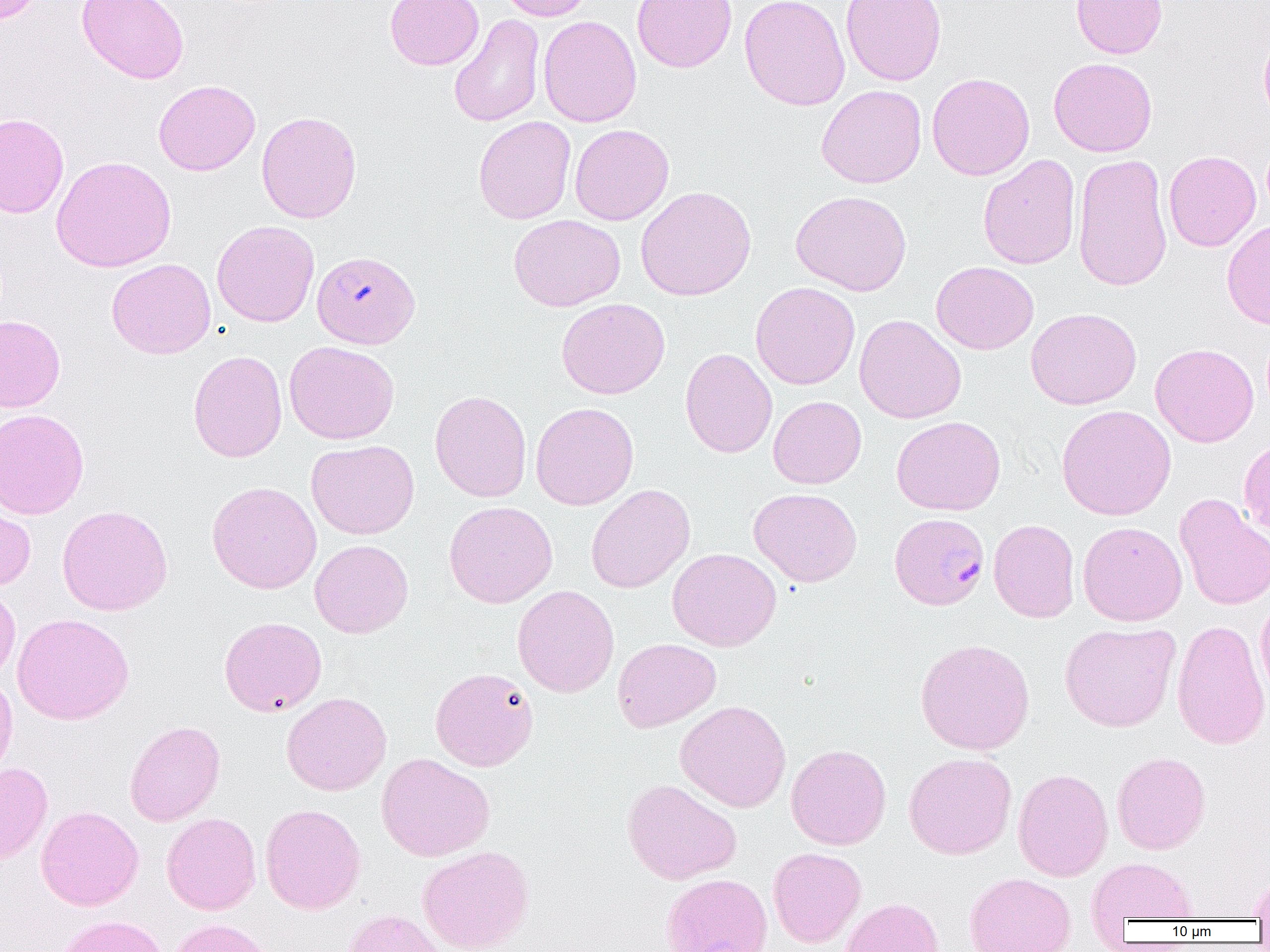

slide_level_diagnosis: Plasmodium falciparum
field_of_view: one of a larger specimen
plasmodium_falciparum_infected_red_blood_cell_locations_subset: 'approximate bounding boxes as [x1, y1, x2, y2] in pixels: [888, 513, 989, 610]'
modality: optical microscopy
preparation: thin blood film
magnification: 1000x
image_size: 1270×952 pixels
uninfected_red_blood_cell_locations_subset: 'approximate bounding boxes as [x1, y1, x2, y2] in pixels: [0, 0, 43, 25], [76, 0, 189, 84], [385, 0, 484, 70], [497, 0, 593, 21], [632, 0, 737, 72], [739, 0, 850, 111], [840, 0, 947, 86], [1071, 0, 1167, 59], [449, 14, 545, 128], [538, 15, 642, 128], [1258, 28, 1270, 127], [1048, 57, 1157, 157], [926, 72, 1035, 181], [154, 79, 261, 176], [816, 84, 927, 188], [256, 111, 362, 224], [0, 113, 69, 218], [473, 116, 576, 224], [569, 124, 674, 225], [1163, 150, 1261, 251], [1072, 153, 1172, 293], [978, 155, 1081, 269], [51, 156, 176, 272], [635, 186, 757, 301], [790, 190, 912, 296], [509, 214, 625, 312], [211, 220, 319, 327], [1221, 220, 1270, 329], [106, 258, 216, 359], [931, 261, 1039, 354], [750, 282, 860, 389], [556, 298, 670, 399], [1026, 307, 1141, 410], [854, 314, 966, 423], [0, 315, 65, 412], [284, 340, 399, 445], [1150, 343, 1259, 447], [679, 348, 777, 458], [188, 350, 287, 462], [430, 390, 532, 502], [768, 396, 866, 489], [530, 402, 639, 510], [1056, 404, 1176, 521], [0, 408, 89, 520], [892, 415, 1005, 516], [1239, 438, 1270, 540], [307, 440, 419, 539], [207, 481, 322, 594], [586, 484, 695, 593], [749, 488, 862, 587], [1173, 494, 1270, 611], [443, 500, 558, 608], [0, 501, 36, 591], [56, 504, 173, 616], [989, 519, 1080, 623], [1077, 521, 1187, 626], [310, 539, 413, 638], [668, 548, 781, 651], [0, 583, 21, 685], [512, 585, 619, 697], [1255, 594, 1270, 705], [12, 613, 134, 725], [218, 616, 327, 716], [1171, 618, 1270, 750], [1059, 621, 1181, 732], [612, 638, 721, 732], [915, 638, 1035, 755], [430, 667, 538, 771], [0, 671, 18, 783], [281, 692, 391, 796], [675, 700, 791, 812], [124, 720, 225, 826], [786, 744, 891, 849], [1111, 751, 1210, 854], [904, 752, 1016, 859], [376, 753, 495, 862], [0, 762, 53, 864], [1012, 768, 1113, 881], [621, 778, 742, 885], [260, 804, 366, 914], [36, 806, 144, 910], [161, 812, 261, 915], [417, 845, 535, 952], [768, 847, 866, 948], [1086, 857, 1198, 926], [964, 872, 1076, 952], [660, 873, 773, 952], [1247, 874, 1270, 920], [840, 897, 945, 952], [339, 909, 448, 952], [55, 915, 168, 952], [167, 918, 274, 952]'